Name the parasite shown.
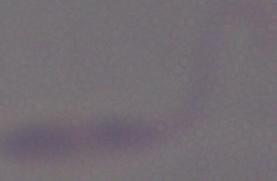

This is Leishmania.

1000x magnification. Photomicrograph.